Give the position of every Plasmodium parasite visible.
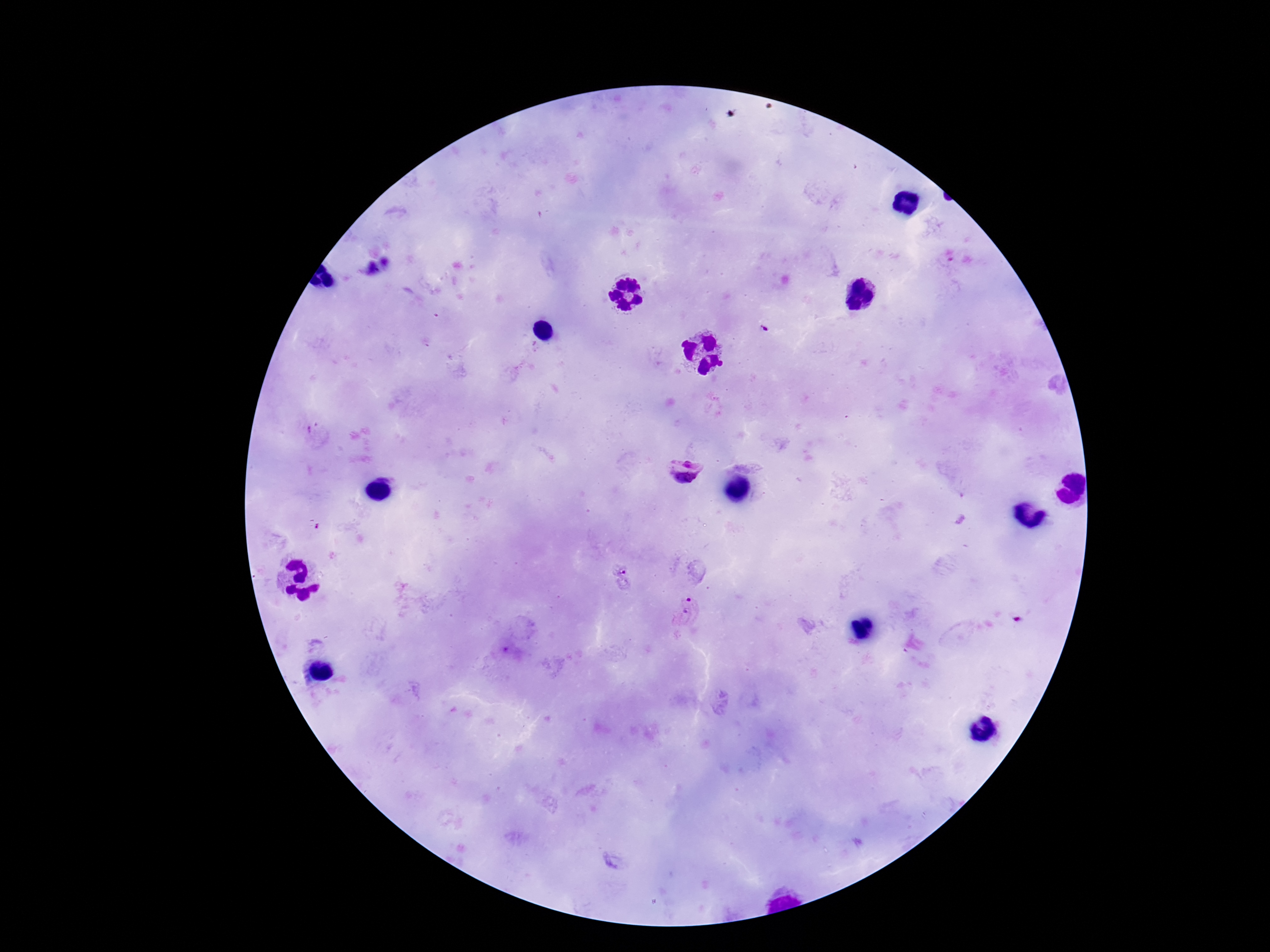

Approximate centers as [x, y] in pixels.
Plasmodium parasites: [386, 262], [371, 269], [764, 329], [688, 462], [682, 486], [623, 576], [687, 610].

Summary:
  - Capture: smartphone camera through the microscope eyepiece
  - Stain: Giemsa
  - Patient malaria status: positive
  - Field of view: single
  - Preparation: thick peripheral-blood smear
  - Image size: 1270×952 pixels
  - Magnification: 100x